Comment on the morphology of the red blood cells.
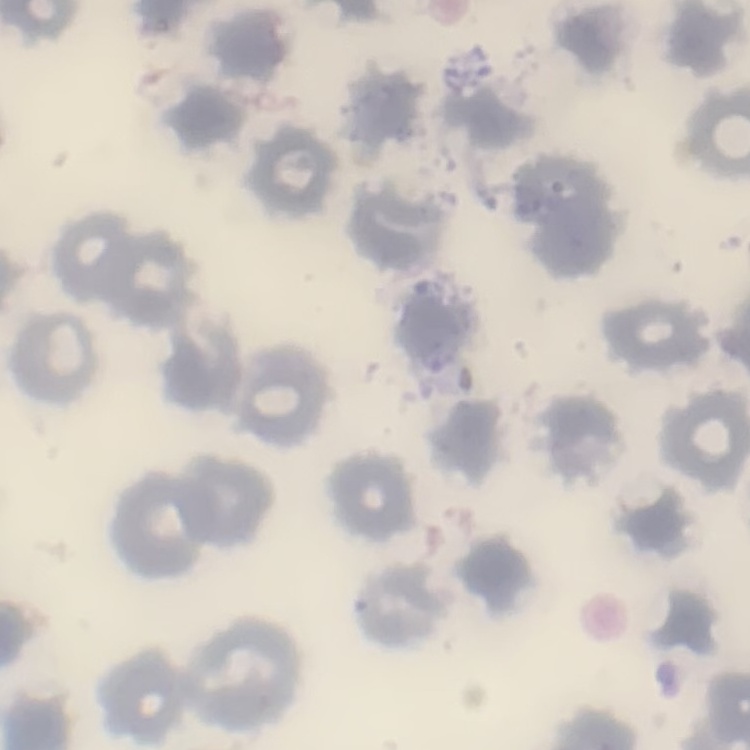
No rouleaux formation.

Summary:
  - Stain: Field's or Giemsa
  - Image type: one tile cut from a larger photomicrograph
  - Preparation: thin blood film